Name the blood parasite species.
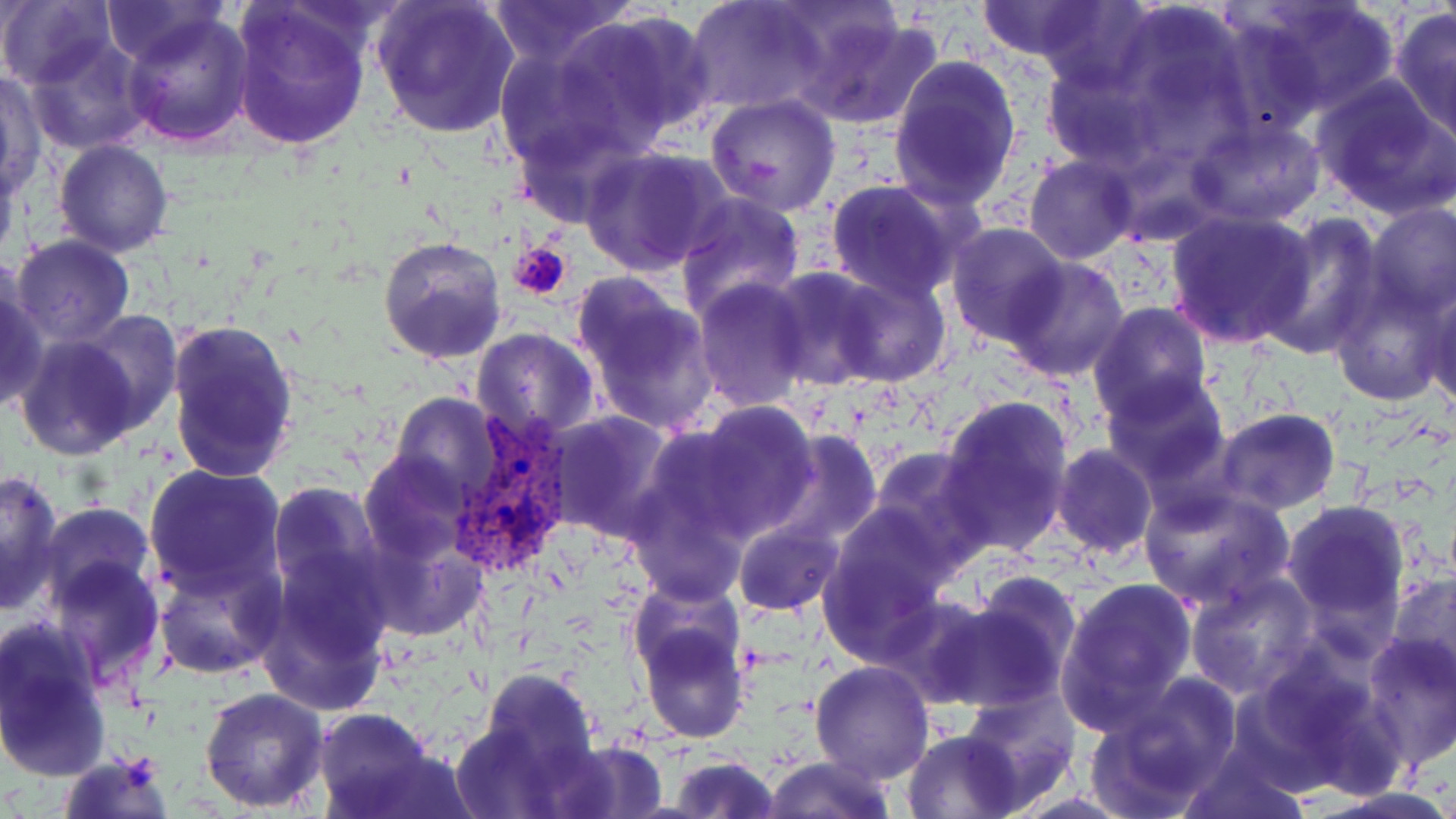
Plasmodium vivax.

Summary:
  - Coordinate format: approximate bounding boxes as named x1/y1/x2/y2 corners in pixels
  - Platelet locations: (x1=511, y1=243, x2=573, y2=301)
  - Plasmodium vivax-infected red blood cell locations: (x1=445, y1=417, x2=580, y2=580)
  - Uninfected red blood cell locations: (x1=102, y1=0, x2=229, y2=66), (x1=228, y1=0, x2=373, y2=149), (x1=372, y1=0, x2=519, y2=140), (x1=488, y1=0, x2=636, y2=66), (x1=686, y1=0, x2=823, y2=115), (x1=972, y1=0, x2=1118, y2=63), (x1=1035, y1=0, x2=1152, y2=95), (x1=1239, y1=0, x2=1402, y2=121), (x1=0, y1=2, x2=115, y2=88), (x1=787, y1=6, x2=942, y2=128), (x1=1097, y1=8, x2=1255, y2=159), (x1=1390, y1=8, x2=1456, y2=143), (x1=122, y1=9, x2=255, y2=146), (x1=563, y1=9, x2=717, y2=149), (x1=23, y1=35, x2=154, y2=154), (x1=494, y1=40, x2=628, y2=171), (x1=888, y1=56, x2=1023, y2=207), (x1=1041, y1=61, x2=1166, y2=170), (x1=1, y1=72, x2=44, y2=197), (x1=1310, y1=76, x2=1456, y2=219), (x1=703, y1=94, x2=844, y2=217), (x1=1188, y1=119, x2=1326, y2=228), (x1=54, y1=139, x2=174, y2=257), (x1=581, y1=147, x2=729, y2=275), (x1=0, y1=149, x2=21, y2=267), (x1=1024, y1=154, x2=1141, y2=264), (x1=824, y1=179, x2=969, y2=301), (x1=673, y1=191, x2=804, y2=321), (x1=1364, y1=202, x2=1455, y2=317), (x1=1165, y1=209, x2=1317, y2=347), (x1=1260, y1=218, x2=1383, y2=357), (x1=946, y1=224, x2=1070, y2=347), (x1=377, y1=234, x2=507, y2=366), (x1=10, y1=235, x2=135, y2=347), (x1=1001, y1=256, x2=1131, y2=383), (x1=766, y1=268, x2=890, y2=389), (x1=826, y1=270, x2=953, y2=387), (x1=0, y1=275, x2=46, y2=413), (x1=1325, y1=277, x2=1451, y2=409), (x1=693, y1=279, x2=812, y2=412), (x1=574, y1=283, x2=718, y2=435), (x1=1424, y1=285, x2=1456, y2=415), (x1=1088, y1=302, x2=1215, y2=422), (x1=69, y1=310, x2=183, y2=436), (x1=165, y1=315, x2=299, y2=485), (x1=471, y1=327, x2=600, y2=443), (x1=14, y1=330, x2=142, y2=459), (x1=1101, y1=372, x2=1232, y2=485), (x1=388, y1=393, x2=503, y2=503), (x1=936, y1=394, x2=1074, y2=557), (x1=684, y1=402, x2=820, y2=541), (x1=1215, y1=407, x2=1340, y2=514), (x1=547, y1=411, x2=677, y2=544), (x1=765, y1=431, x2=884, y2=550), (x1=1051, y1=445, x2=1157, y2=560), (x1=865, y1=448, x2=989, y2=569), (x1=359, y1=451, x2=472, y2=562), (x1=626, y1=458, x2=754, y2=604), (x1=142, y1=462, x2=289, y2=596), (x1=0, y1=469, x2=65, y2=612), (x1=268, y1=481, x2=385, y2=599), (x1=1138, y1=485, x2=1296, y2=614), (x1=1283, y1=501, x2=1410, y2=632), (x1=38, y1=504, x2=155, y2=608), (x1=821, y1=517, x2=952, y2=659), (x1=732, y1=518, x2=842, y2=617), (x1=359, y1=525, x2=485, y2=643), (x1=43, y1=554, x2=165, y2=689), (x1=259, y1=554, x2=395, y2=715), (x1=152, y1=557, x2=280, y2=680), (x1=1185, y1=571, x2=1318, y2=700), (x1=1386, y1=571, x2=1456, y2=689), (x1=1056, y1=576, x2=1198, y2=731), (x1=628, y1=578, x2=745, y2=688), (x1=930, y1=583, x2=1079, y2=712), (x1=634, y1=612, x2=750, y2=745), (x1=0, y1=619, x2=111, y2=780), (x1=1360, y1=632, x2=1456, y2=768), (x1=1237, y1=648, x2=1411, y2=794), (x1=811, y1=660, x2=935, y2=784), (x1=475, y1=666, x2=601, y2=781), (x1=1087, y1=677, x2=1242, y2=817), (x1=199, y1=687, x2=329, y2=812), (x1=958, y1=687, x2=1081, y2=803), (x1=315, y1=708, x2=433, y2=815), (x1=453, y1=719, x2=578, y2=819), (x1=903, y1=729, x2=1026, y2=818), (x1=545, y1=739, x2=669, y2=817), (x1=1175, y1=745, x2=1313, y2=819), (x1=57, y1=751, x2=176, y2=819), (x1=667, y1=755, x2=780, y2=819), (x1=761, y1=755, x2=898, y2=819), (x1=1306, y1=787, x2=1456, y2=819)
  - Field of view: one of a larger specimen
  - Preparation: thin blood film
  - Magnification: 1000x
  - Stain: May-Grünwald-Giemsa
  - Image size: 1456×819 pixels
  - Modality: optical microscopy